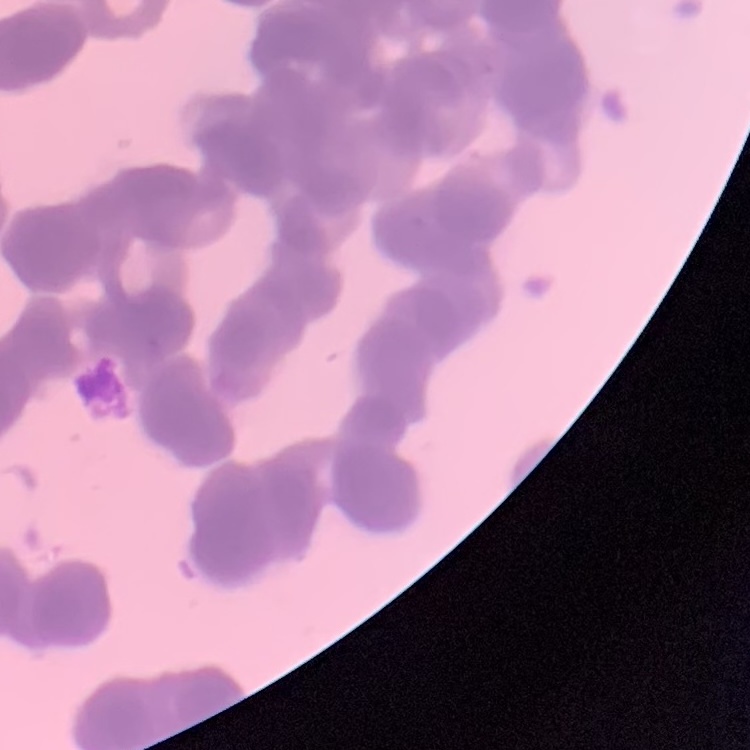 The red blood cells exhibit rouleaux formation. Square crop of a larger photomicrograph. Thin blood smear. Field's or Giemsa stain.